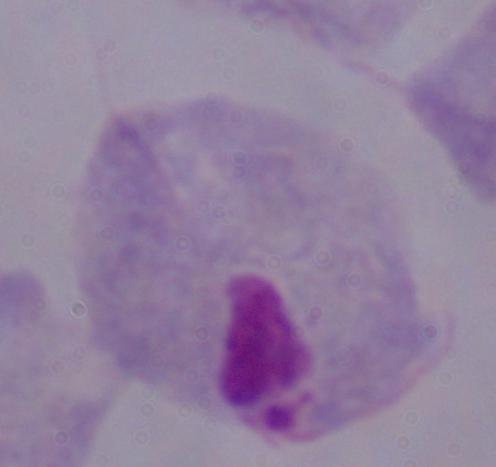

Summary:
  - Magnification: 1000x
  - Modality: micrograph
  - Identification: trichomonad